Assess this cell for malaria.
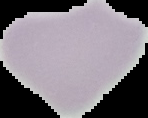

Uninfected.

image_size: 148×118 pixels
image_type: cell region segmented out of the field of view; surrounding area masked to black
preparation: thin blood smear